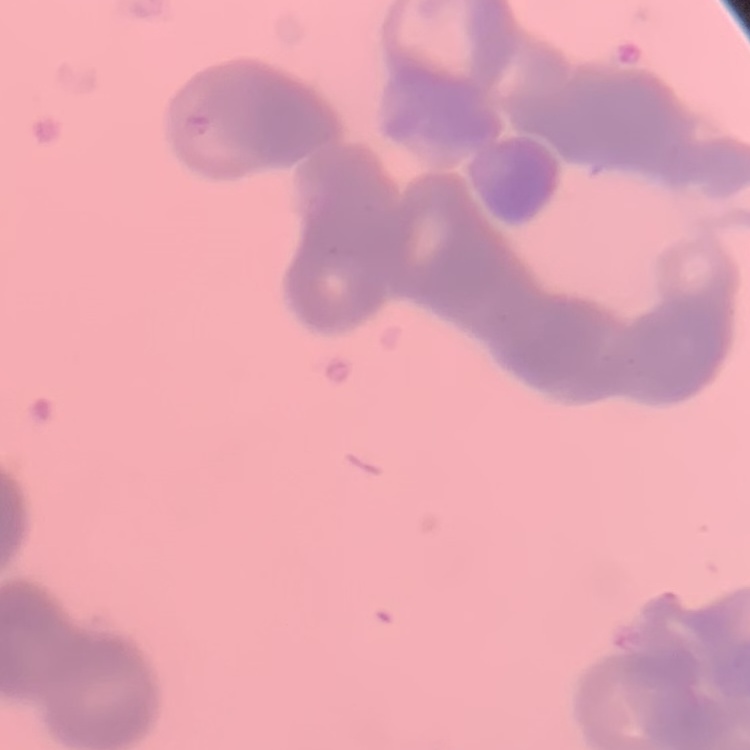
{
  "red_blood_cell_morphology": "rouleaux formation",
  "preparation": "thin blood film",
  "stain": "Field's or Giemsa",
  "image_type": "square crop of a larger photomicrograph"
}